Describe the morphology of the red blood cells.
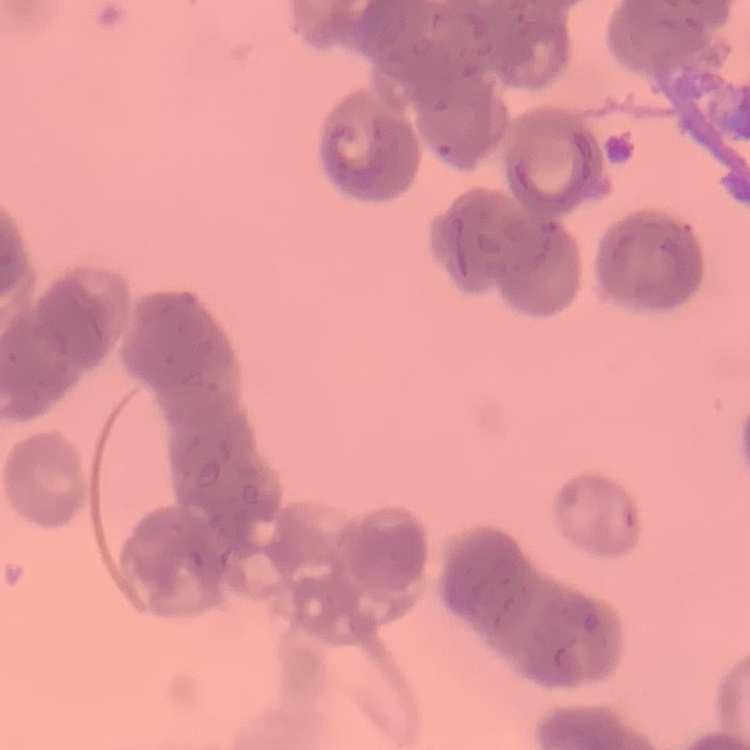

They show rouleaux formation.

Thin blood film. Field's or Giemsa stain. Square crop of a larger photomicrograph.